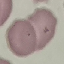

Summary:
  - Malaria status: uninfected
  - Capture: smartphone through the microscope eyepiece
  - Image type: cell patch, automatically extracted from a larger field of view and resized to 64 × 64 pixels
  - Stain: Giemsa
  - Preparation: thin blood smear